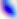
modality = photomicrograph
magnification = 400x
identification = Toxoplasma gondii